Describe the morphology of the red blood cells.
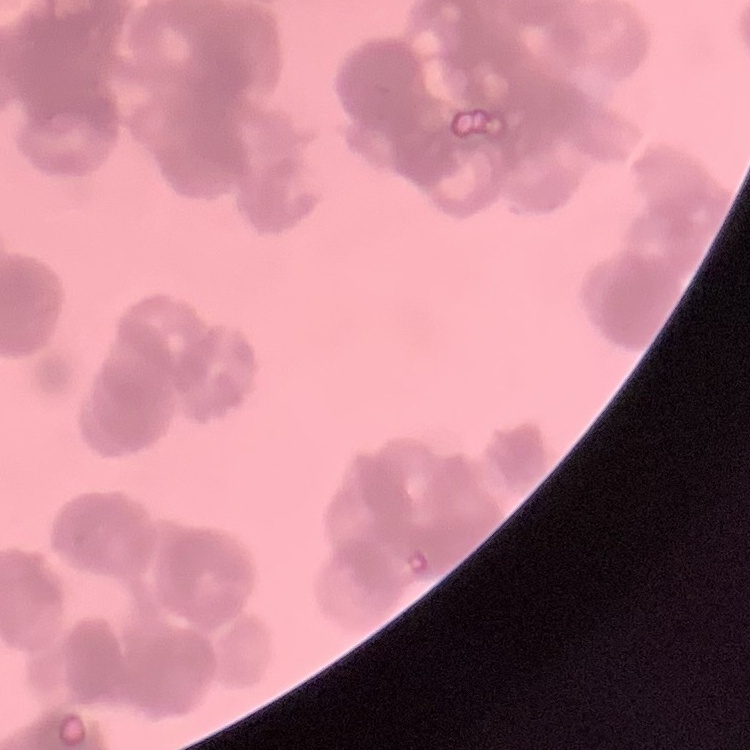
Rouleaux formation.

Thin peripheral smear. Square crop of a larger photomicrograph. Field's or Giemsa stain.